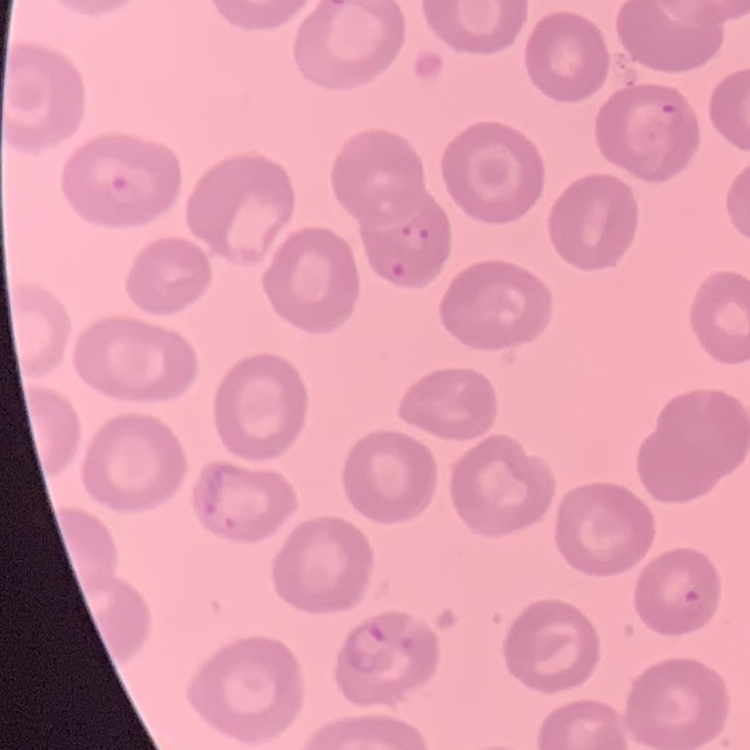
Summary:
  - Red blood cell morphology: no rouleaux formation
  - Preparation: thin peripheral smear
  - Stain: Field's or Giemsa
  - Image type: square crop of a larger photomicrograph